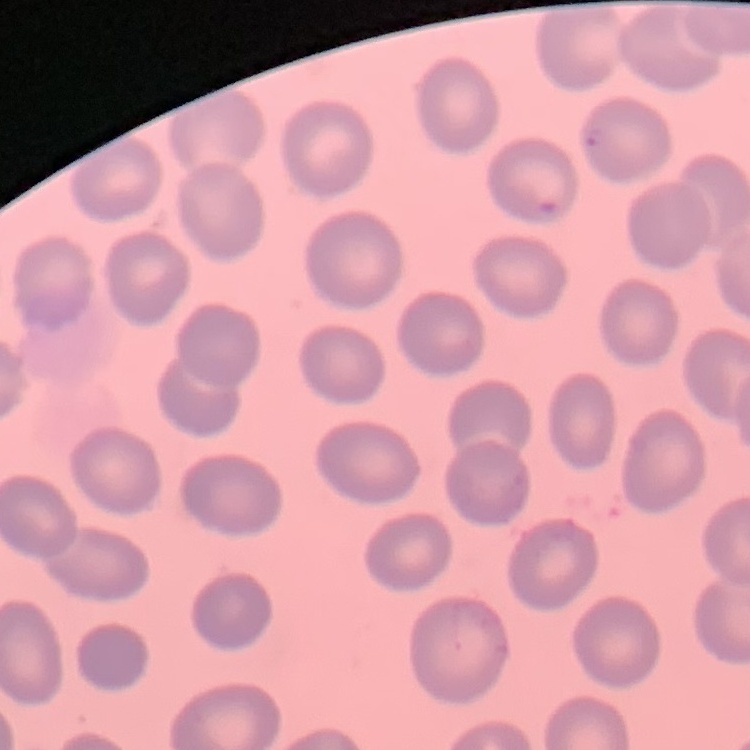

The red blood cells show no rouleaux formation. Field's or Giemsa stain. Square crop of a larger photomicrograph. Thin peripheral smear.